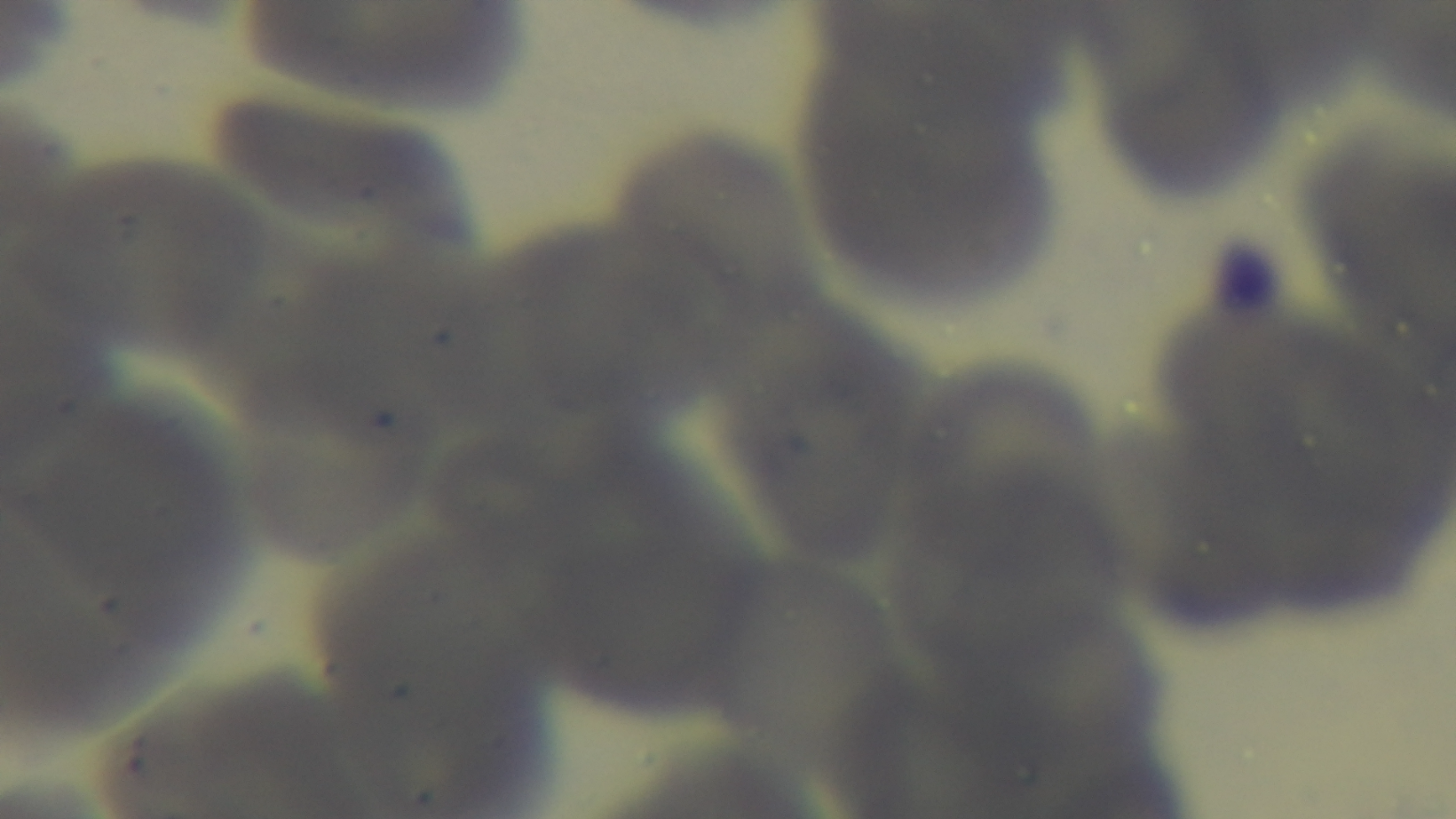

Summary:
  - Malaria status: negative
  - Stain: Giemsa
  - Objective: 100x oil immersion
  - Field of view: one from the slide
  - Preparation: thin smear
  - Capture: mounted 4K digital camera
  - Modality: light microscopy